Assess this cell for malaria.
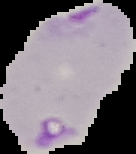

It is parasitized.

Segmented cell region on a black background. From a thin blood film. Image is 136×154 pixels.